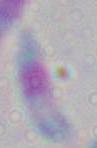
identification = Toxoplasma gondii
modality = micrograph
magnification = 1000x